Locate every blood parasite and identify its species.
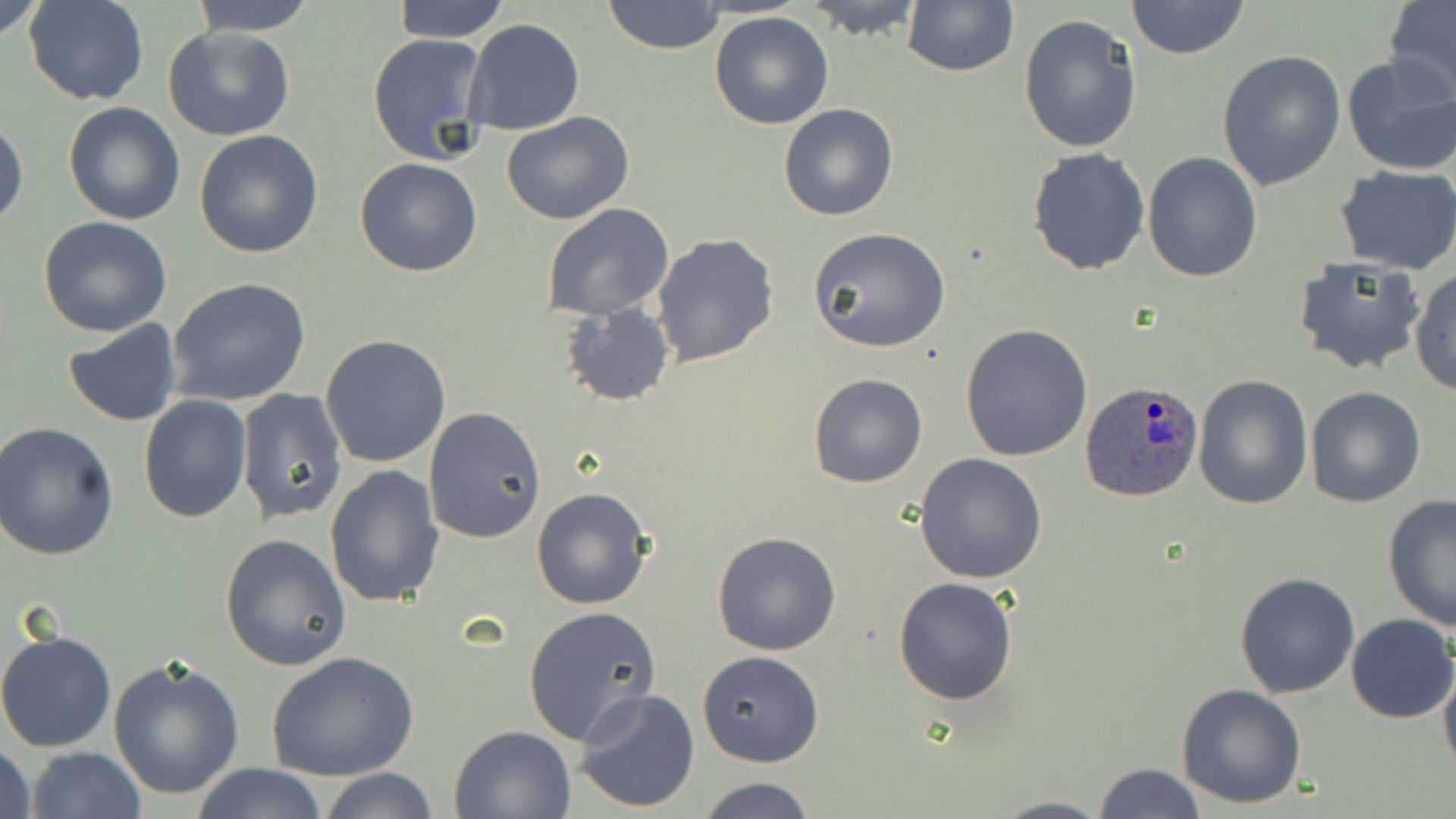

Approximate bounding boxes as [x1, y1, x2, y2] in pixels.
Plasmodium ovale-infected red blood cells: [1081, 383, 1206, 505].
No Plasmodium falciparum, Plasmodium malariae, Plasmodium vivax, Babesia divergens, or Trypanosoma brucei observed.

Uninfected red blood cell locations: [0, 0, 51, 45], [24, 0, 148, 106], [391, 0, 510, 42], [601, 0, 727, 55], [804, 0, 925, 41], [1125, 0, 1250, 60], [190, 1, 318, 36], [901, 1, 1019, 77], [1383, 1, 1456, 99], [709, 11, 834, 130], [1018, 14, 1143, 156], [462, 19, 585, 136], [161, 26, 297, 143], [367, 31, 494, 167], [1340, 50, 1456, 177], [1217, 51, 1346, 190], [63, 102, 185, 225], [778, 103, 899, 221], [501, 112, 634, 225], [0, 114, 27, 230], [193, 129, 325, 260], [1026, 147, 1151, 277], [1143, 150, 1263, 283], [355, 157, 483, 277], [1335, 165, 1456, 274], [542, 202, 675, 321], [38, 218, 172, 337], [808, 226, 950, 352], [651, 233, 779, 367], [1293, 257, 1426, 376], [1410, 266, 1456, 396], [167, 277, 311, 406], [559, 302, 675, 408], [62, 318, 183, 426], [961, 324, 1093, 464], [320, 334, 453, 469], [1191, 373, 1313, 510], [809, 374, 927, 488], [1306, 386, 1425, 507], [237, 388, 348, 526], [137, 395, 252, 521], [422, 407, 545, 544], [2, 421, 120, 561], [914, 452, 1047, 585], [324, 466, 446, 609], [532, 488, 653, 609], [1382, 494, 1456, 632], [712, 531, 842, 656], [219, 533, 351, 670], [1234, 571, 1361, 699], [892, 577, 1018, 704], [523, 605, 660, 745], [1344, 614, 1456, 723], [0, 629, 119, 754], [696, 650, 824, 768], [266, 651, 419, 781], [107, 655, 245, 801], [1438, 656, 1456, 780], [1176, 682, 1308, 809], [572, 688, 700, 813], [450, 724, 578, 818], [0, 741, 36, 819], [24, 746, 145, 819], [191, 763, 328, 818], [1091, 763, 1205, 819], [319, 767, 439, 819], [698, 776, 817, 818], [989, 794, 1112, 819]. Slide-level diagnosis: Plasmodium ovale. May-Grünwald-Giemsa stain. Thin blood film. One field of a larger specimen. 1000x magnification. Optical microscopy. Image is 1456×819 pixels.